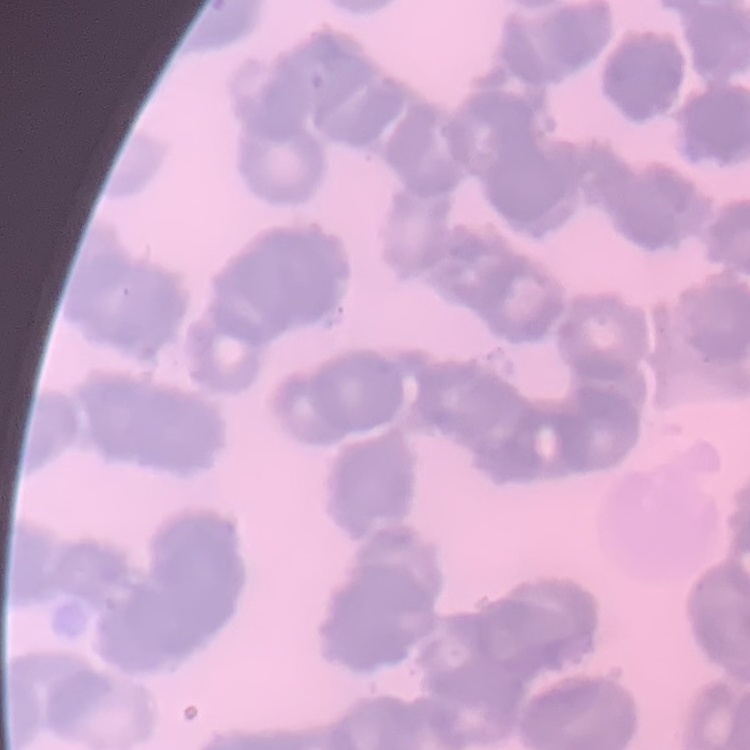
Summary:
  - Red blood cell morphology: rouleaux formation
  - Preparation: thin peripheral smear
  - Stain: Field's or Giemsa
  - Image type: one tile cut from a larger photomicrograph